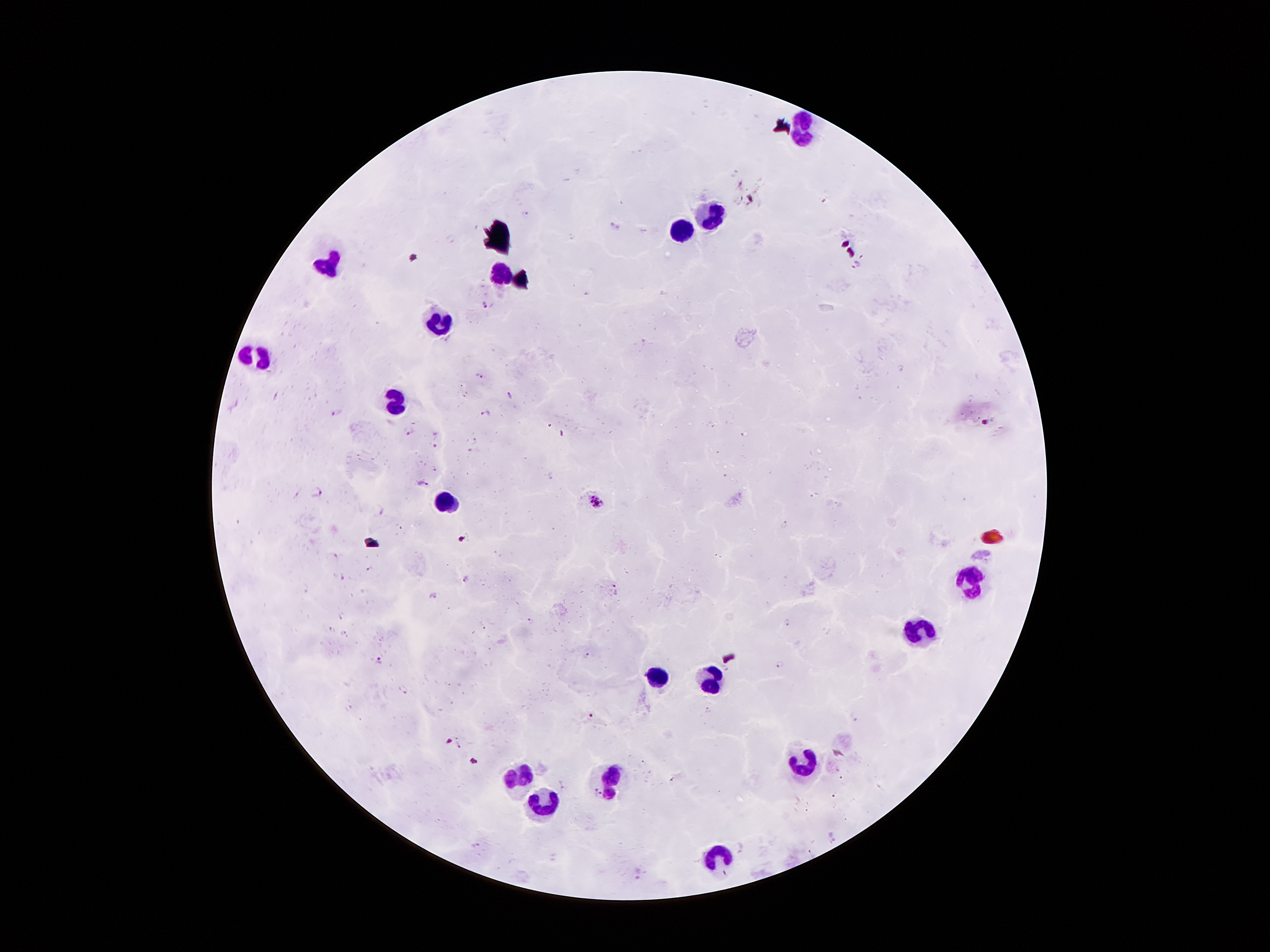

Approximate centers as [x, y] in pixels. Leukocyte locations: [809, 134], [714, 216], [685, 230], [326, 259], [499, 276], [443, 322], [260, 360], [398, 404], [449, 505], [971, 582], [923, 628], [657, 680], [711, 681], [808, 767], [514, 776], [613, 778], [536, 811], [718, 857]. Malaria parasite locations: [858, 264], [486, 304], [480, 376], [510, 394], [486, 413], [338, 414], [411, 432], [436, 446], [435, 468], [423, 483], [318, 492], [596, 501], [370, 568], [467, 578], [344, 579], [614, 585], [435, 596], [343, 617], [532, 621], [788, 623], [331, 629], [345, 632], [588, 655], [379, 661], [781, 662], [402, 690], [708, 709], [591, 717], [856, 717], [841, 777], [672, 780], [835, 796], [477, 846]. 100x magnification. Patient malaria status: positive for Plasmodium falciparum. Giemsa-stained preparation. One field from this slide. Thick peripheral-blood smear. Image is 1270×952 pixels. Photographed through the microscope eyepiece with a smartphone camera.